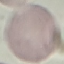
Malaria status: uninfected. Giemsa-stained preparation. Acquired by smartphone through the microscope eyepiece. Thin blood smear. Automatically extracted cell patch, resized to 64 × 64 pixels.